Name the parasite shown.
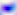
This is Toxoplasma gondii.

Summary:
  - Magnification: 400x
  - Modality: photomicrograph